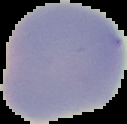
{
  "result": "negative for malaria parasites",
  "image_type": "segmented cell region on a black background",
  "image_size": "127×124 pixels",
  "preparation": "thin blood film"
}